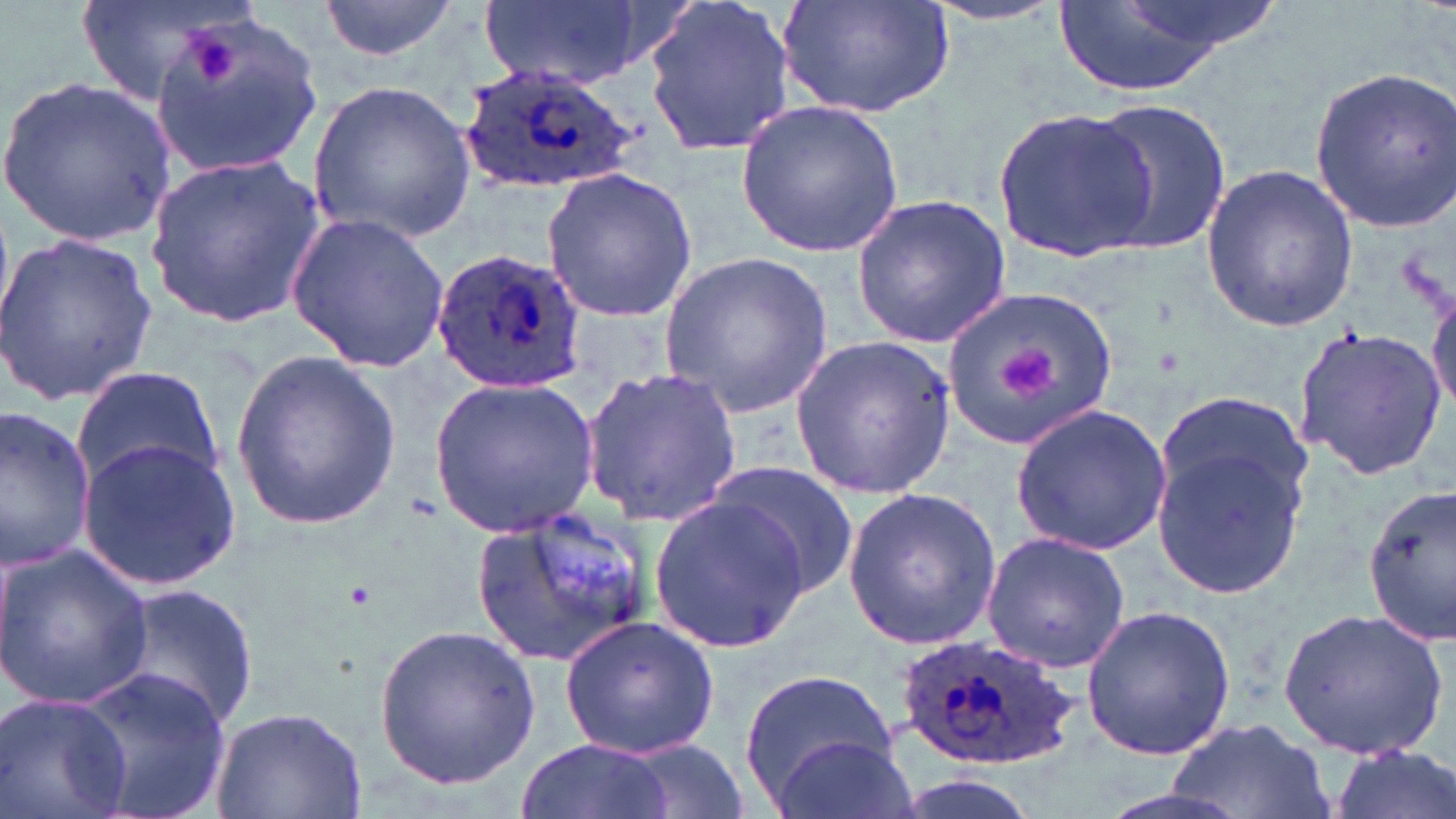

slide-level diagnosis = Plasmodium ovale
modality = optical microscopy
magnification = 1000x
field of view = single
Plasmodium ovale-infected red blood cell locations = approximate bounding boxes as (x1,y1)-(x2,y2) corner pairs in pixels: (457,63)-(639,193), (428,247)-(589,395), (893,633)-(1082,769)
uninfected red blood cell locations = approximate bounding boxes as (x1,y1)-(x2,y2) corner pairs in pixels: (73,0)-(257,106), (318,0)-(458,63), (477,0)-(649,88), (642,0)-(798,159), (779,0)-(959,118), (1051,0)-(1244,96), (920,1)-(1072,27), (151,13)-(326,178), (1307,65)-(1456,232), (2,75)-(174,247), (306,80)-(476,244), (1084,98)-(1231,253), (737,101)-(904,259), (994,109)-(1155,260), (145,154)-(324,328), (1200,163)-(1359,334), (541,167)-(699,322), (849,193)-(1013,348), (287,212)-(450,370), (0,232)-(156,405), (661,249)-(833,417), (1427,278)-(1456,416), (946,286)-(1119,448), (1294,324)-(1444,480), (788,335)-(956,500), (228,352)-(405,527), (71,365)-(224,494), (581,365)-(743,524), (428,374)-(603,534), (1010,403)-(1174,556), (0,406)-(97,570), (1152,421)-(1313,599), (77,438)-(241,588), (705,462)-(858,595), (1362,484)-(1455,641), (841,488)-(1001,650), (648,494)-(812,653), (473,512)-(654,663), (981,532)-(1132,675), (0,542)-(154,709), (107,582)-(258,733), (1080,603)-(1238,760), (1276,607)-(1452,762), (558,615)-(721,761), (372,620)-(542,791), (72,665)-(228,819), (738,666)-(896,804), (1,691)-(133,819), (210,703)-(368,819), (1164,716)-(1330,819), (770,734)-(918,819), (514,735)-(675,819), (611,738)-(757,817), (1329,745)-(1455,819), (884,771)-(1047,819), (1088,783)-(1256,819)
image size = 1456×819 pixels
stain = May-Grünwald-Giemsa
preparation = thin blood smear
platelet locations = approximate bounding boxes as (x1,y1)-(x2,y2) corner pairs in pixels: (182,27)-(238,84), (998,342)-(1062,409)